Assess this cell for malaria.
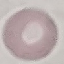
Uninfected.

Summary:
  - Capture: smartphone through the microscope eyepiece
  - Preparation: thin smear
  - Stain: Giemsa
  - Image type: automatically extracted cell patch, resized to 64 × 64 pixels